Outline each blood parasite and name the species.
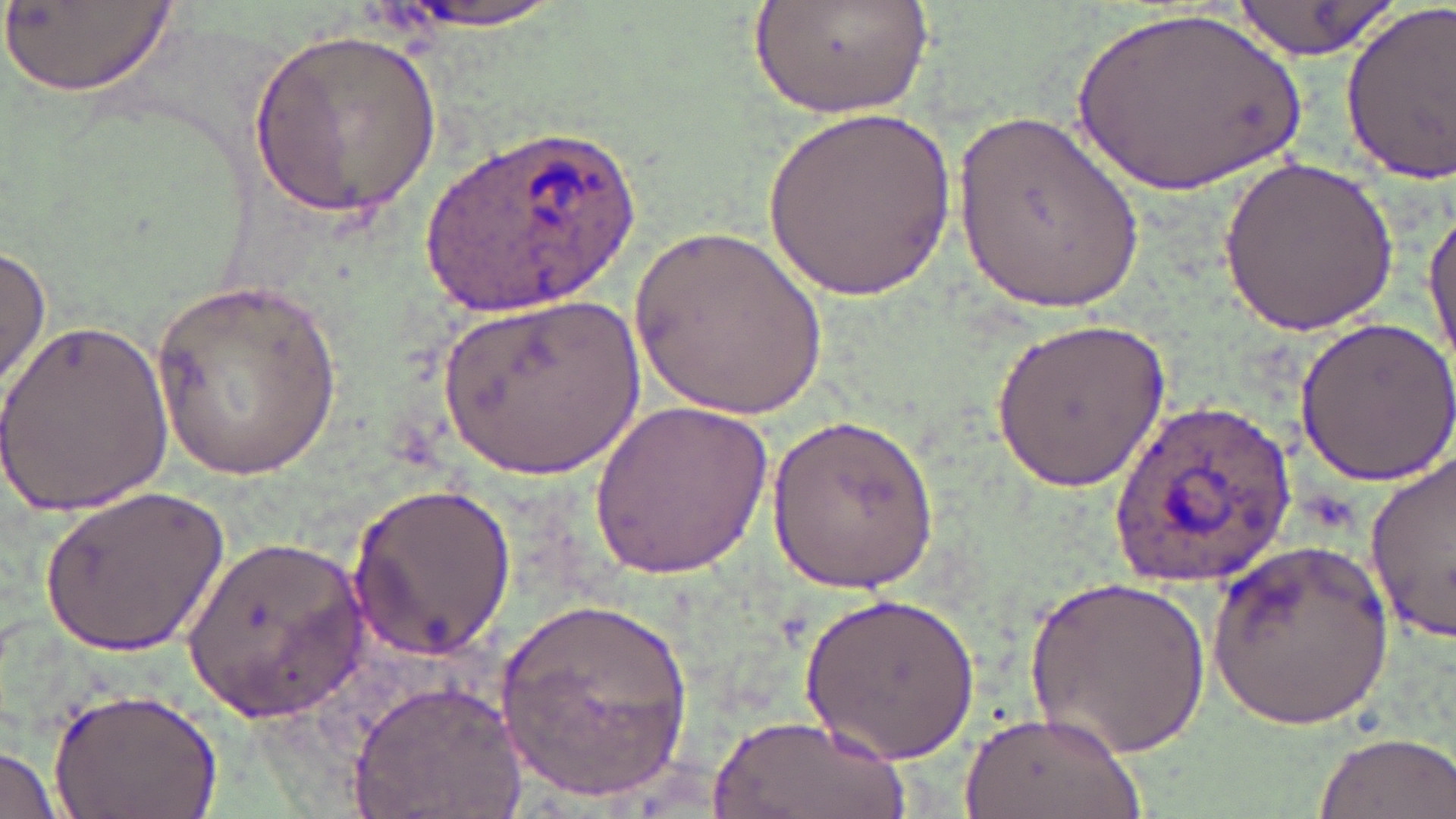

Approximate bounding boxes as [x1, y1, x2, y2] in pixels.
Plasmodium ovale-infected red blood cells: [419, 123, 642, 314], [1105, 396, 1296, 586].
No Plasmodium falciparum, Plasmodium malariae, Plasmodium vivax, Babesia divergens, or Trypanosoma brucei observed.

Summary:
  - Uninfected red blood cell locations: [5, 0, 176, 100], [382, 0, 578, 31], [749, 0, 935, 117], [1229, 0, 1395, 60], [1337, 0, 1456, 190], [1065, 3, 1312, 203], [250, 30, 440, 221], [949, 104, 1144, 316], [764, 105, 954, 306], [1217, 155, 1398, 338], [1423, 194, 1456, 380], [631, 218, 828, 421], [0, 244, 51, 392], [150, 280, 344, 484], [429, 286, 650, 487], [0, 316, 173, 519], [1294, 316, 1456, 485], [988, 317, 1171, 493], [594, 400, 776, 576], [767, 415, 939, 595], [1362, 454, 1456, 641], [346, 482, 521, 657], [44, 483, 229, 658], [181, 534, 370, 716], [1209, 538, 1394, 732], [1025, 574, 1209, 762], [499, 591, 697, 799], [801, 592, 980, 765], [350, 678, 526, 819], [48, 687, 221, 819], [957, 708, 1142, 819], [707, 712, 909, 819], [1314, 730, 1454, 819], [0, 742, 64, 819]
  - Slide-level diagnosis: Plasmodium ovale
  - Field of view: one of a larger specimen
  - Magnification: 1000x
  - Preparation: thin blood smear
  - Image size: 1456×819 pixels
  - Stain: May-Grünwald-Giemsa
  - Modality: optical microscopy